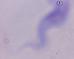

Summary:
  - Modality: micrograph
  - Magnification: 1000x
  - Identification: trypanosome